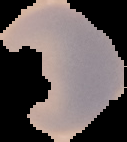
Summary:
  - Image type: segmented cell region on a black background
  - Result: no malaria parasites seen
  - Preparation: thin blood film
  - Image size: 127×142 pixels